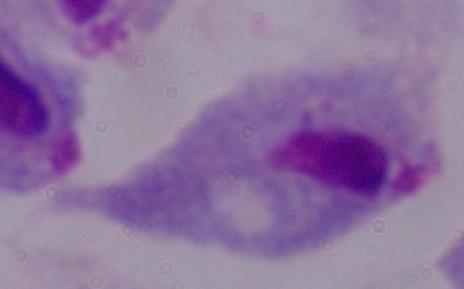 A trichomonad is shown. Captured at 1000x magnification. Photomicrograph.